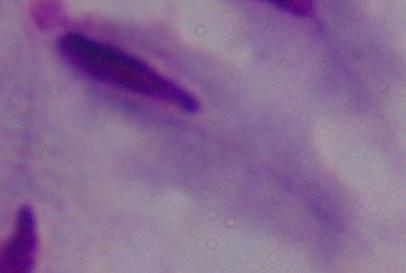
modality = micrograph
identification = trichomonad
magnification = 1000x